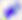

Summary:
  - Modality: photomicrograph
  - Magnification: 400x
  - Identification: Toxoplasma gondii